Outline each Babesia divergens-infected red blood cell.
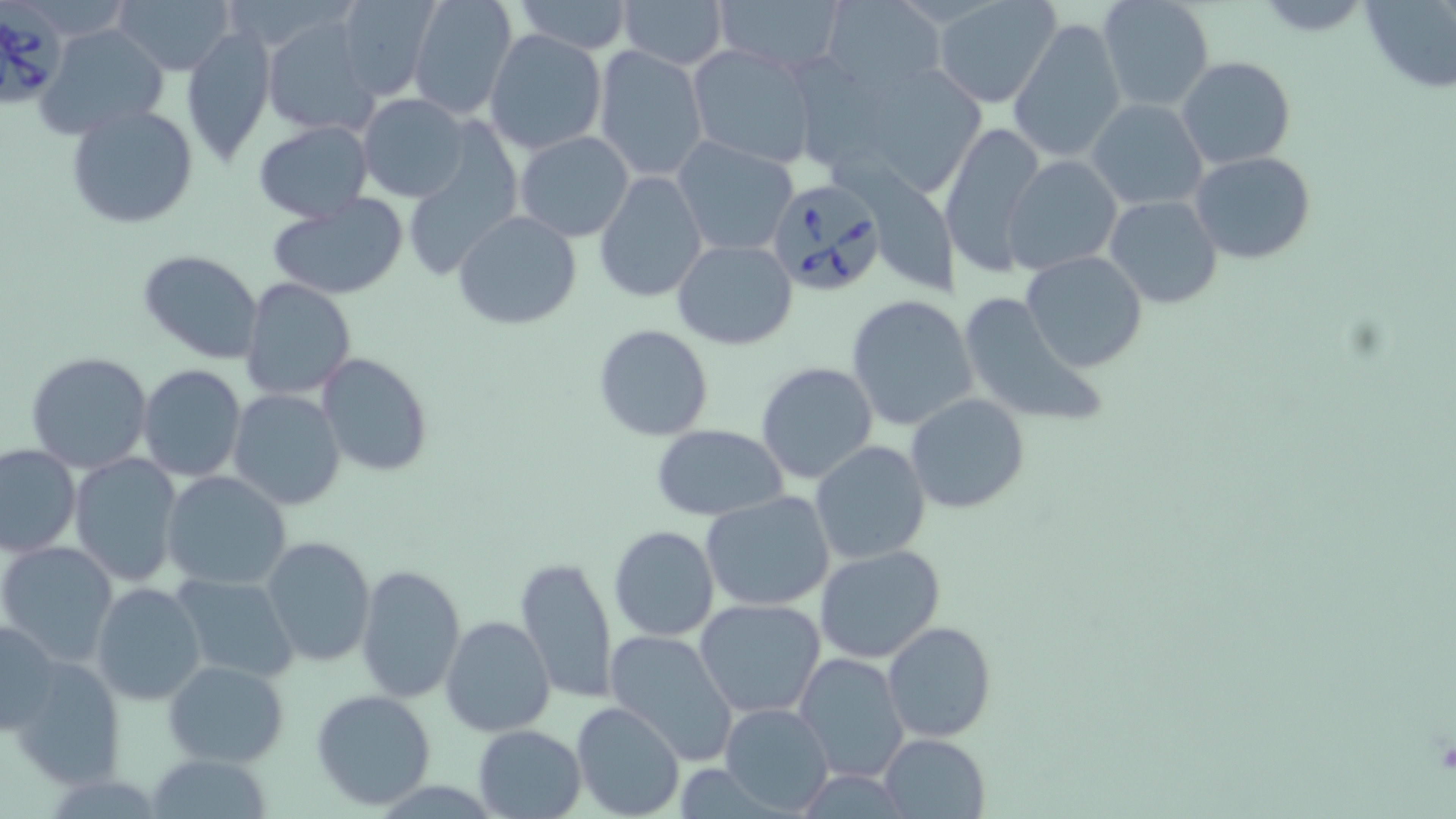
Approximate bounding boxes as [x1, y1, x2, y2] in pixels.
Babesia divergens-infected red blood cells: [0, 1, 66, 108], [764, 177, 887, 298].

Uninfected red blood cell locations: [118, 0, 234, 73], [332, 0, 438, 100], [510, 0, 635, 54], [614, 0, 727, 68], [715, 0, 847, 74], [822, 0, 946, 95], [933, 0, 1062, 109], [1097, 0, 1215, 111], [1359, 0, 1456, 91], [408, 2, 518, 121], [263, 14, 379, 137], [1009, 14, 1127, 162], [38, 23, 170, 143], [180, 24, 275, 166], [484, 29, 607, 156], [686, 43, 821, 169], [593, 45, 709, 184], [1176, 57, 1296, 171], [829, 60, 971, 193], [357, 93, 470, 203], [1087, 99, 1208, 210], [67, 104, 199, 229], [253, 121, 374, 222], [940, 122, 1045, 278], [400, 125, 523, 278], [516, 130, 633, 241], [673, 138, 798, 257], [1191, 151, 1316, 265], [840, 156, 965, 289], [1003, 156, 1122, 274], [594, 173, 707, 302], [266, 194, 411, 299], [1105, 194, 1222, 309], [453, 210, 582, 330], [672, 238, 798, 349], [137, 250, 263, 364], [1021, 251, 1148, 371], [242, 278, 357, 402], [958, 290, 1108, 428], [847, 295, 979, 433], [592, 325, 714, 442], [25, 350, 153, 473], [317, 353, 434, 477], [755, 361, 880, 485], [137, 364, 247, 482], [228, 389, 347, 512], [906, 394, 1032, 514], [651, 423, 787, 522], [810, 440, 931, 565], [0, 444, 82, 557], [70, 453, 182, 586], [160, 470, 292, 590], [701, 489, 835, 612], [609, 525, 719, 641], [261, 536, 377, 667], [0, 540, 119, 666], [814, 545, 946, 663], [514, 554, 618, 705], [355, 564, 467, 703], [169, 573, 300, 682], [90, 581, 207, 705], [694, 599, 825, 719], [441, 615, 555, 738], [1, 616, 62, 736], [883, 620, 997, 741], [605, 630, 740, 766], [795, 652, 909, 782], [8, 656, 127, 787], [163, 660, 290, 767], [310, 688, 438, 811], [571, 701, 684, 819], [720, 703, 833, 814], [472, 725, 586, 817], [878, 733, 989, 819], [145, 755, 276, 817]. Slide-level diagnosis: Babesia divergens. May-Grünwald-Giemsa-stained preparation. Image is 1456×819 pixels. Thin blood smear. 1000x magnification. Single field of view. Light microscopy.